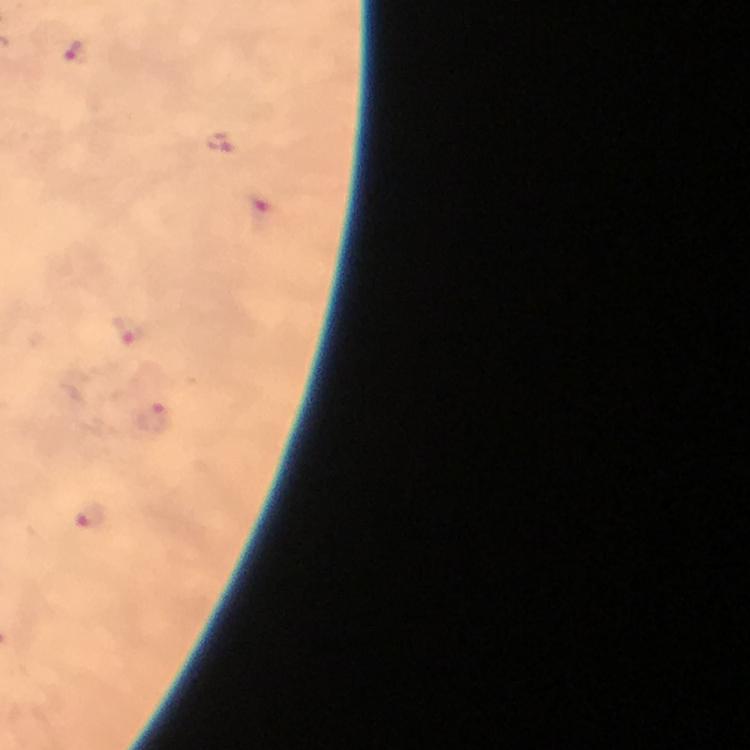

Approximate centers as (x, y) in pixels.
Summary:
  - Malaria parasite locations: (76, 51), (222, 143), (262, 215), (125, 329), (152, 417), (90, 515)
  - Preparation: thick blood smear
  - Cropped from: a single field of view
  - Context: from a malaria diagnostic workup
  - Image size: 750×750 pixels
  - Immersion oil: applied
  - Stain: Giemsa
  - Capture: smartphone mounted on the microscope
  - Magnification: 100x